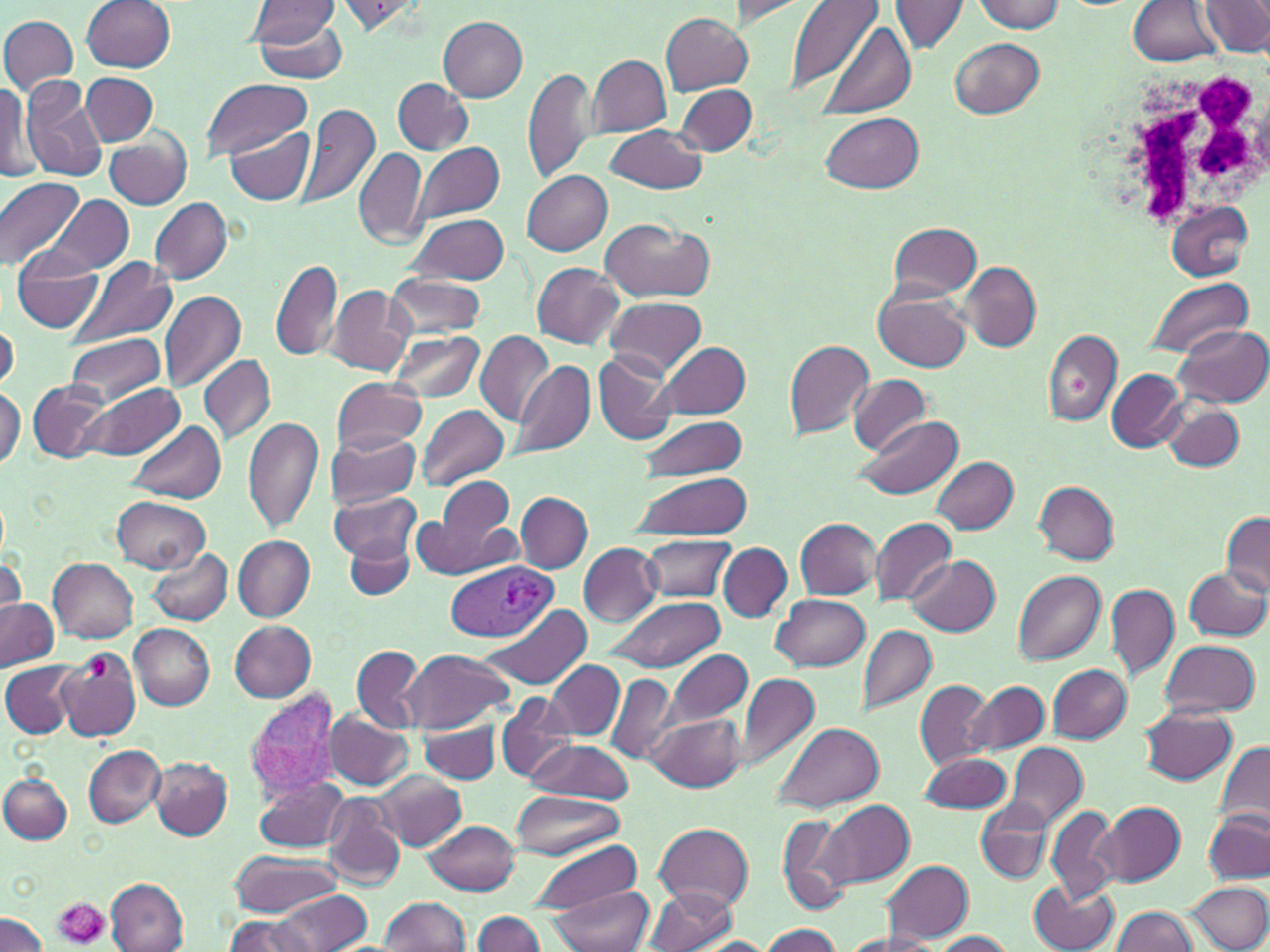

Summary:
  - Coordinate format: approximate bounding boxes as named x1/y1/x2/y2 corners in pixels
  - Plasmodium vivax-infected red blood cell locations: (x1=441, y1=560, x2=556, y2=642), (x1=242, y1=689, x2=341, y2=809)
  - Platelet locations: (x1=87, y1=655, x2=113, y2=683), (x1=51, y1=899, x2=111, y2=950)
  - Uninfected red blood cell locations: (x1=82, y1=0, x2=176, y2=73), (x1=787, y1=0, x2=883, y2=95), (x1=1200, y1=0, x2=1269, y2=56), (x1=248, y1=1, x2=341, y2=47), (x1=334, y1=1, x2=428, y2=36), (x1=728, y1=1, x2=809, y2=26), (x1=890, y1=1, x2=967, y2=56), (x1=973, y1=1, x2=1064, y2=33), (x1=1126, y1=1, x2=1221, y2=66), (x1=250, y1=10, x2=350, y2=85), (x1=662, y1=13, x2=752, y2=94), (x1=0, y1=15, x2=79, y2=96), (x1=438, y1=15, x2=528, y2=102), (x1=819, y1=23, x2=915, y2=118), (x1=950, y1=36, x2=1044, y2=118), (x1=589, y1=55, x2=670, y2=137), (x1=522, y1=67, x2=597, y2=184), (x1=81, y1=72, x2=158, y2=145), (x1=392, y1=78, x2=472, y2=155), (x1=0, y1=79, x2=33, y2=186), (x1=199, y1=79, x2=314, y2=163), (x1=20, y1=82, x2=109, y2=183), (x1=675, y1=85, x2=757, y2=154), (x1=297, y1=103, x2=380, y2=211), (x1=821, y1=111, x2=922, y2=194), (x1=603, y1=124, x2=706, y2=194), (x1=223, y1=125, x2=312, y2=204), (x1=106, y1=131, x2=192, y2=211), (x1=415, y1=141, x2=503, y2=221), (x1=353, y1=147, x2=429, y2=250), (x1=522, y1=170, x2=612, y2=256), (x1=0, y1=178, x2=84, y2=270), (x1=44, y1=193, x2=134, y2=276), (x1=151, y1=197, x2=233, y2=286), (x1=1165, y1=201, x2=1253, y2=281), (x1=405, y1=212, x2=512, y2=285), (x1=599, y1=218, x2=714, y2=303), (x1=887, y1=221, x2=983, y2=299), (x1=12, y1=250, x2=103, y2=334), (x1=70, y1=255, x2=177, y2=349), (x1=271, y1=259, x2=343, y2=362), (x1=532, y1=262, x2=623, y2=349), (x1=962, y1=262, x2=1041, y2=350), (x1=385, y1=274, x2=484, y2=339), (x1=1143, y1=277, x2=1255, y2=358), (x1=322, y1=284, x2=414, y2=377), (x1=873, y1=289, x2=972, y2=374), (x1=159, y1=290, x2=246, y2=392), (x1=605, y1=296, x2=704, y2=375), (x1=1, y1=324, x2=18, y2=391), (x1=1172, y1=325, x2=1270, y2=408), (x1=386, y1=329, x2=484, y2=405), (x1=1042, y1=329, x2=1122, y2=425), (x1=64, y1=330, x2=165, y2=406), (x1=475, y1=331, x2=555, y2=427), (x1=784, y1=337, x2=875, y2=440), (x1=654, y1=341, x2=751, y2=420), (x1=592, y1=349, x2=678, y2=447), (x1=200, y1=353, x2=275, y2=446), (x1=512, y1=361, x2=595, y2=459), (x1=1106, y1=369, x2=1188, y2=452), (x1=848, y1=375, x2=932, y2=456), (x1=332, y1=377, x2=428, y2=455), (x1=28, y1=379, x2=114, y2=465), (x1=84, y1=384, x2=183, y2=461), (x1=0, y1=388, x2=24, y2=469), (x1=1161, y1=400, x2=1245, y2=473), (x1=417, y1=404, x2=509, y2=491), (x1=243, y1=416, x2=323, y2=534), (x1=638, y1=416, x2=748, y2=481), (x1=855, y1=416, x2=962, y2=501), (x1=129, y1=421, x2=226, y2=503), (x1=327, y1=432, x2=422, y2=508), (x1=932, y1=456, x2=1019, y2=533), (x1=627, y1=473, x2=751, y2=540), (x1=424, y1=478, x2=518, y2=574), (x1=1034, y1=481, x2=1118, y2=564), (x1=328, y1=491, x2=421, y2=563), (x1=516, y1=492, x2=592, y2=573), (x1=113, y1=496, x2=209, y2=573), (x1=1220, y1=511, x2=1270, y2=597), (x1=871, y1=516, x2=956, y2=606), (x1=795, y1=518, x2=880, y2=599), (x1=640, y1=534, x2=734, y2=601), (x1=234, y1=535, x2=314, y2=621), (x1=344, y1=537, x2=413, y2=599), (x1=579, y1=543, x2=661, y2=626), (x1=719, y1=543, x2=792, y2=621), (x1=149, y1=548, x2=233, y2=626), (x1=0, y1=554, x2=24, y2=621), (x1=905, y1=555, x2=1001, y2=637), (x1=49, y1=558, x2=139, y2=642), (x1=1184, y1=566, x2=1269, y2=641), (x1=1012, y1=569, x2=1105, y2=664), (x1=1105, y1=583, x2=1180, y2=679), (x1=605, y1=594, x2=727, y2=674), (x1=773, y1=594, x2=869, y2=671), (x1=0, y1=597, x2=57, y2=670), (x1=480, y1=603, x2=592, y2=689), (x1=230, y1=620, x2=317, y2=701), (x1=130, y1=624, x2=214, y2=711), (x1=856, y1=625, x2=937, y2=716), (x1=1160, y1=638, x2=1261, y2=718), (x1=350, y1=644, x2=428, y2=733), (x1=403, y1=648, x2=512, y2=732), (x1=661, y1=648, x2=753, y2=731), (x1=57, y1=650, x2=142, y2=740), (x1=2, y1=661, x2=79, y2=738), (x1=546, y1=661, x2=625, y2=739), (x1=1046, y1=663, x2=1131, y2=743), (x1=737, y1=674, x2=819, y2=770), (x1=607, y1=676, x2=679, y2=764), (x1=915, y1=679, x2=994, y2=770), (x1=965, y1=679, x2=1049, y2=756), (x1=495, y1=691, x2=576, y2=785), (x1=1138, y1=706, x2=1239, y2=786), (x1=647, y1=711, x2=745, y2=791), (x1=323, y1=712, x2=413, y2=789), (x1=418, y1=720, x2=498, y2=783), (x1=772, y1=721, x2=885, y2=814), (x1=527, y1=738, x2=634, y2=802), (x1=1003, y1=741, x2=1088, y2=833), (x1=1215, y1=741, x2=1270, y2=832), (x1=82, y1=745, x2=165, y2=826), (x1=917, y1=752, x2=1012, y2=813), (x1=148, y1=756, x2=233, y2=839), (x1=375, y1=772, x2=465, y2=850), (x1=0, y1=774, x2=72, y2=844), (x1=251, y1=777, x2=351, y2=851), (x1=322, y1=792, x2=406, y2=888), (x1=509, y1=792, x2=623, y2=859), (x1=819, y1=799, x2=913, y2=889), (x1=977, y1=800, x2=1053, y2=883), (x1=1095, y1=801, x2=1185, y2=887), (x1=1044, y1=805, x2=1118, y2=903), (x1=1203, y1=808, x2=1270, y2=884), (x1=775, y1=815, x2=853, y2=912), (x1=423, y1=819, x2=520, y2=895), (x1=655, y1=823, x2=753, y2=911), (x1=528, y1=839, x2=644, y2=916), (x1=229, y1=849, x2=338, y2=916), (x1=882, y1=859, x2=974, y2=942), (x1=107, y1=878, x2=188, y2=952), (x1=1030, y1=882, x2=1119, y2=952), (x1=1188, y1=882, x2=1270, y2=951), (x1=546, y1=885, x2=654, y2=952), (x1=645, y1=886, x2=738, y2=952), (x1=273, y1=890, x2=371, y2=951), (x1=378, y1=896, x2=468, y2=951), (x1=1111, y1=907, x2=1196, y2=952), (x1=473, y1=910, x2=546, y2=952), (x1=0, y1=911, x2=47, y2=952), (x1=224, y1=913, x2=314, y2=952), (x1=758, y1=925, x2=841, y2=952), (x1=928, y1=930, x2=1015, y2=951), (x1=834, y1=932, x2=939, y2=951), (x1=696, y1=937, x2=772, y2=952)
  - White blood cell locations: (x1=1101, y1=60, x2=1270, y2=231)
  - Slide-level diagnosis: Plasmodium vivax
  - Image size: 1270×952 pixels
  - Magnification: 1000x
  - Modality: light microscopy
  - Field of view: single
  - Stain: May-Grünwald-Giemsa
  - Preparation: thin blood smear